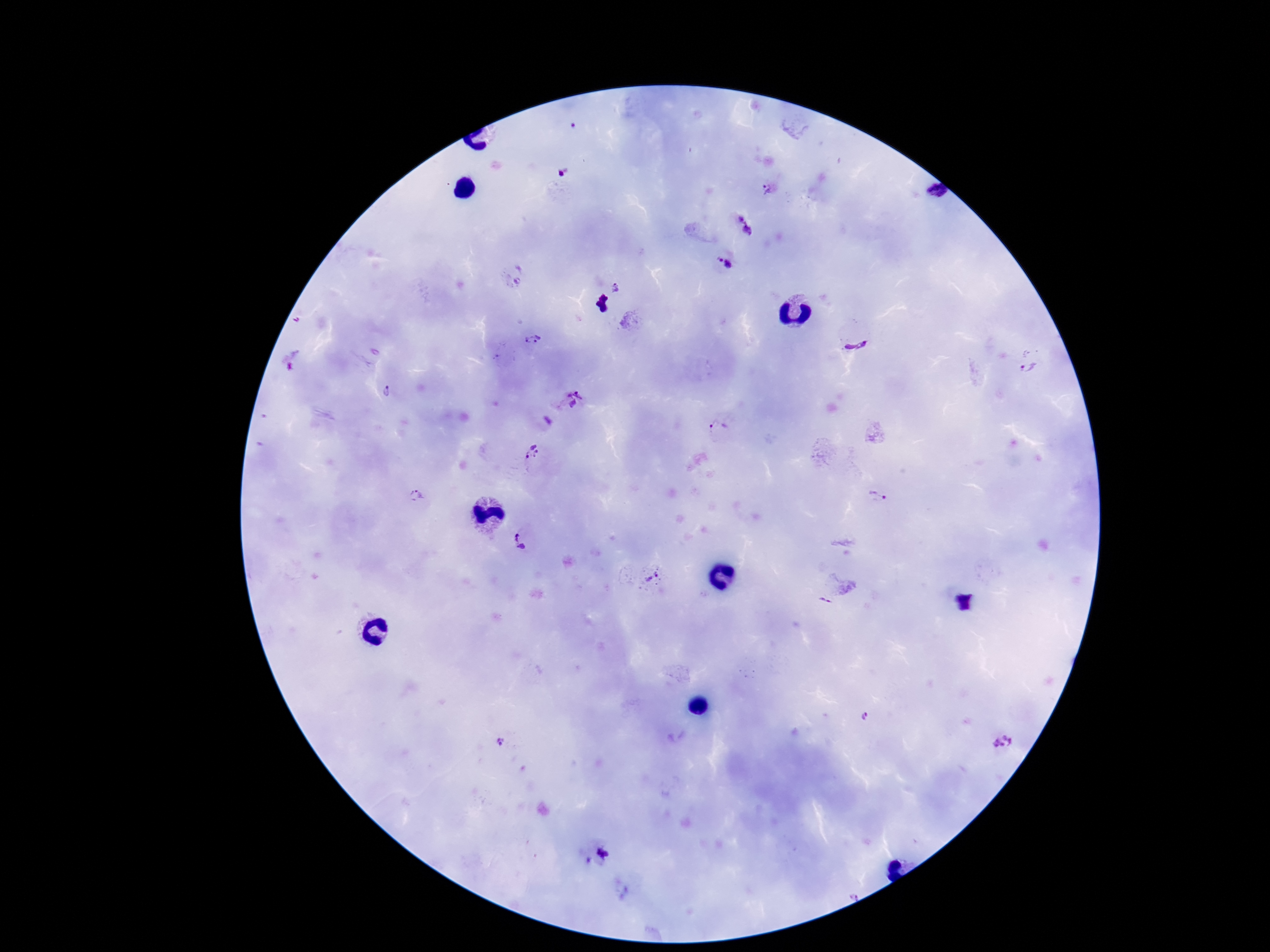

Approximate object centers, in pixels from the top-left corner. Plasmodium parasite locations: (x=769, y=192), (x=747, y=225), (x=726, y=261), (x=516, y=276), (x=617, y=288), (x=856, y=339), (x=534, y=340), (x=293, y=360), (x=1029, y=369), (x=388, y=392), (x=570, y=398), (x=548, y=421), (x=718, y=427), (x=531, y=452), (x=416, y=497), (x=878, y=499), (x=521, y=539), (x=650, y=577), (x=825, y=599), (x=865, y=715), (x=500, y=742), (x=1003, y=742), (x=597, y=857). One field from this slide. Smartphone photograph taken through the microscope eyepiece. Image is 1270×952 pixels. Patient malaria status: positive. 100x magnification. Thick blood film. Giemsa stain.